Point out each Plasmodium parasite.
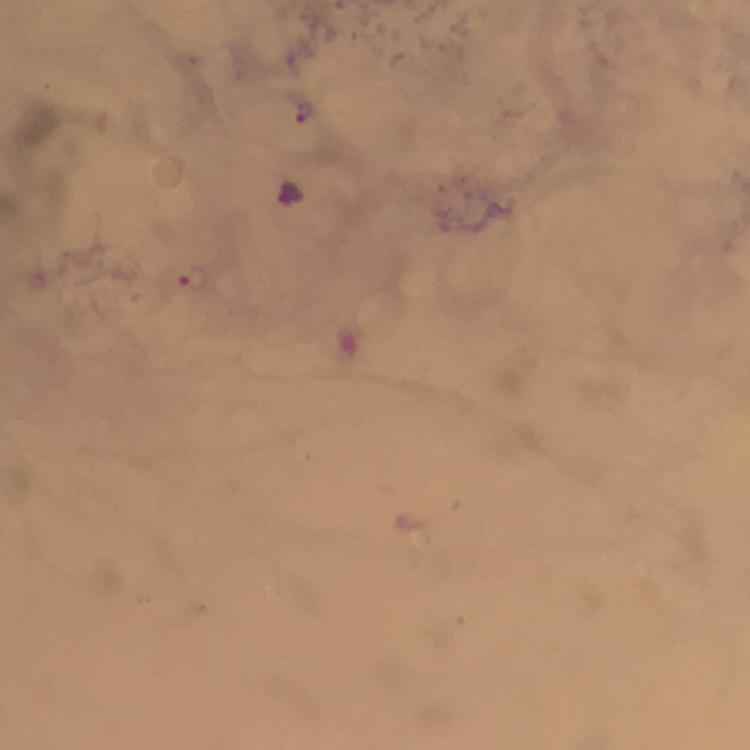

Approximate centers as {x, y} in pixels.
Plasmodium parasites: {305, 113}, {193, 276}.

Photographed through the microscope with a smartphone camera. At 100x magnification. Cropped region of a single field of view. Thick smear. Image is 750×750 pixels. Immersion oil was used. Giemsa stain. From a malaria diagnostic workup.